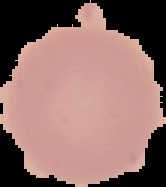
image type = cell region segmented out of the field of view; surrounding area masked to black
image size = 166×187 pixels
malaria status = uninfected
preparation = thin blood smear